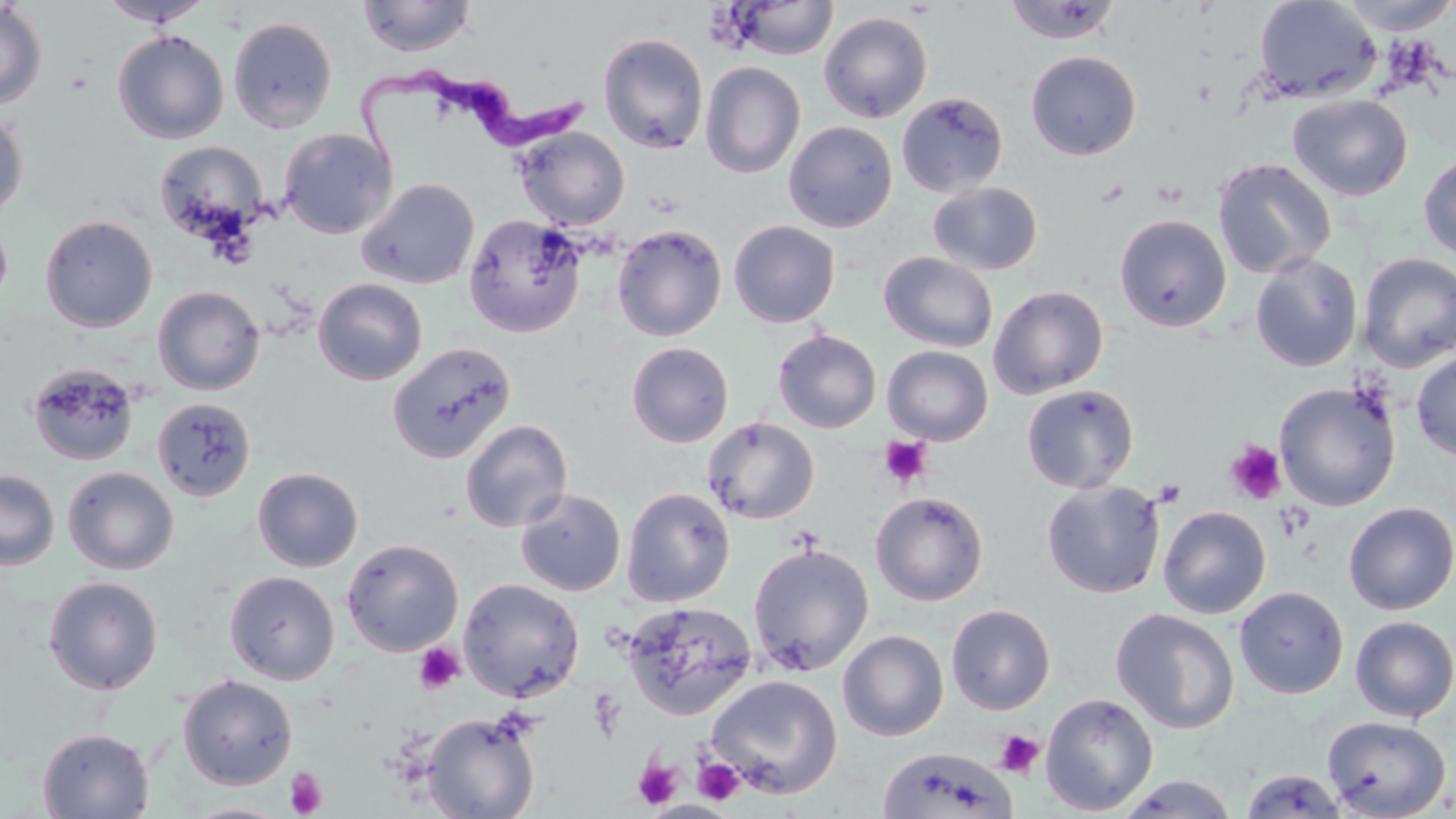

Approximate bounding boxes as (x1, y1, x2, y2) in pixels. Trypanosoma brucei locations: (355, 61, 589, 171). Platelet locations: (879, 436, 933, 489), (1225, 440, 1287, 505), (1154, 479, 1187, 506), (1274, 502, 1313, 541), (414, 643, 465, 694), (993, 729, 1045, 778), (692, 756, 745, 805), (634, 758, 683, 809), (286, 767, 328, 817). Uninfected red blood cell locations: (357, 0, 476, 58), (1253, 0, 1383, 103), (1335, 0, 1456, 35), (0, 1, 47, 110), (99, 1, 213, 26), (727, 1, 838, 60), (1003, 1, 1123, 45), (819, 11, 933, 123), (228, 17, 337, 133), (112, 29, 229, 144), (598, 33, 708, 153), (1026, 51, 1141, 160), (700, 61, 805, 179), (896, 92, 1008, 197), (1287, 94, 1412, 201), (0, 109, 28, 217), (783, 121, 898, 233), (514, 127, 629, 230), (279, 128, 398, 239), (154, 140, 269, 242), (1419, 154, 1456, 261), (1213, 158, 1336, 279), (356, 178, 479, 290), (928, 182, 1043, 275), (0, 212, 14, 312), (463, 213, 587, 338), (1115, 214, 1231, 332), (40, 215, 158, 333), (729, 220, 840, 328), (612, 224, 727, 341), (879, 252, 998, 352), (1358, 252, 1456, 373), (1250, 254, 1362, 372), (313, 277, 428, 385), (153, 285, 264, 395), (989, 285, 1109, 398), (773, 329, 881, 433), (626, 341, 734, 447), (388, 342, 516, 463), (882, 345, 993, 445), (1412, 349, 1456, 461), (27, 362, 140, 467), (1274, 382, 1401, 511), (1021, 384, 1139, 493), (152, 397, 257, 502), (702, 416, 819, 524), (460, 419, 573, 532), (252, 466, 363, 572), (63, 467, 179, 575), (0, 468, 58, 570), (1042, 480, 1165, 599), (621, 487, 735, 607), (515, 488, 626, 597), (870, 491, 989, 606), (1343, 502, 1456, 614), (1158, 506, 1271, 618), (341, 538, 464, 656), (748, 542, 874, 676), (224, 570, 340, 685), (43, 576, 163, 695), (458, 578, 585, 702), (1234, 586, 1349, 699), (621, 601, 758, 720), (946, 604, 1056, 715), (1111, 608, 1240, 735), (1350, 616, 1456, 722), (838, 629, 949, 741), (177, 674, 298, 790), (707, 674, 843, 799), (1040, 692, 1158, 815), (423, 712, 540, 819), (1322, 715, 1451, 819), (36, 727, 155, 818), (877, 746, 1019, 819), (1239, 768, 1348, 817), (1116, 774, 1239, 818), (179, 802, 291, 819). Slide-level diagnosis: Trypanosoma brucei. Image is 1456×819 pixels. Single field of view. Captured at 1000x magnification. Thin blood film. May-Grünwald-Giemsa stain. Optical microscopy.